Classify this cell by malaria status.
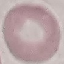
Uninfected.

Summary:
  - Image type: cell patch, automatically extracted from a larger field of view and resized to 64 × 64 pixels
  - Capture: smartphone through the microscope eyepiece
  - Preparation: thin blood smear
  - Stain: Giemsa